Classify this cell by malaria status.
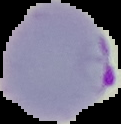

It is parasitized.

Summary:
  - Preparation: thin blood smear
  - Image size: 121×124 pixels
  - Image type: cell region segmented out of the field of view; surrounding area masked to black